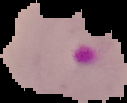

preparation: thin blood smear
image_type: cell region segmented out of the field of view; surrounding area masked to black
image_size: 127×103 pixels
result: malaria parasites detected